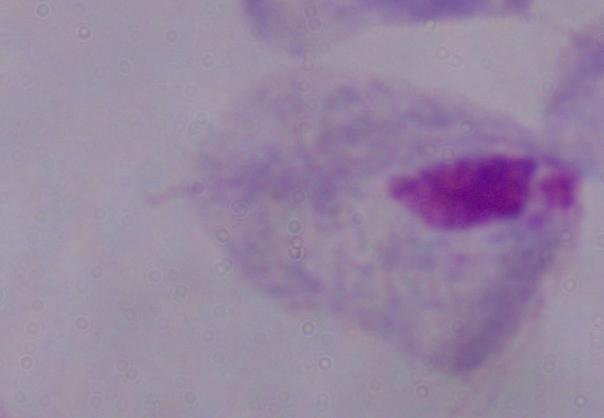

Summary:
  - Modality: micrograph
  - Identification: trichomonad
  - Magnification: 1000x